Give the position of every malaria parasite and every leukocyte.
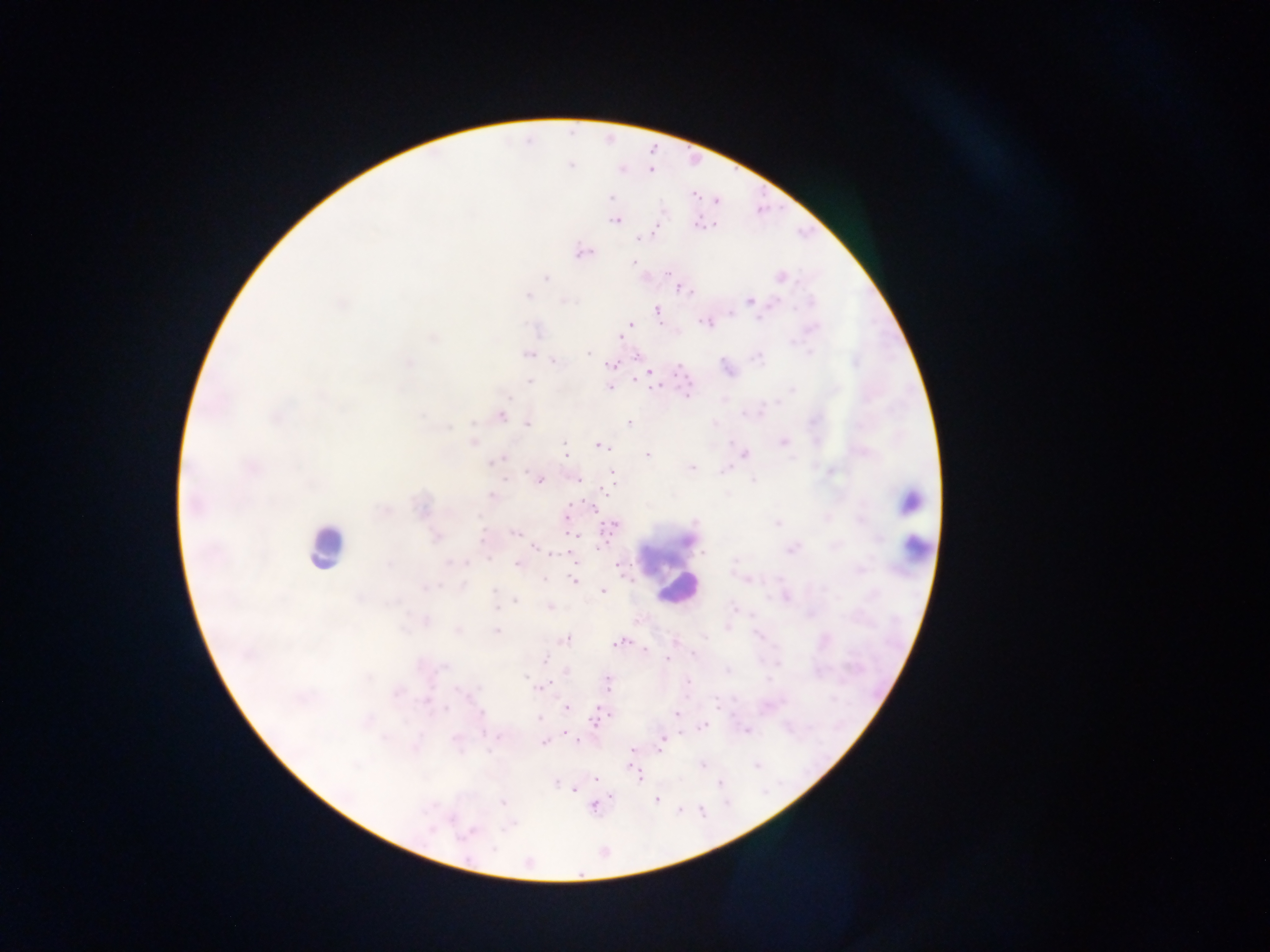
Approximate centers as (x, y) in pixels.
Malaria parasites: (571, 166), (650, 172), (611, 197), (694, 198), (616, 220), (698, 220), (653, 235), (637, 239), (583, 251), (633, 262), (680, 292), (750, 299), (657, 310), (732, 312), (760, 320), (630, 323), (622, 338), (590, 352), (534, 354), (757, 357), (554, 362), (610, 365), (650, 374), (528, 382), (654, 387), (609, 388), (687, 394), (502, 417), (528, 423), (629, 424), (564, 446), (601, 447), (566, 454), (746, 455), (647, 456), (693, 467), (613, 472), (505, 480), (542, 481), (578, 481), (607, 492), (908, 502), (592, 509), (567, 517), (860, 520), (611, 526), (514, 534), (570, 536), (877, 540), (482, 541), (602, 546), (534, 547), (701, 553), (489, 559), (572, 562), (516, 565), (618, 565), (545, 580), (573, 582), (496, 589), (426, 590), (603, 591), (514, 600), (550, 606), (496, 609), (496, 630), (627, 638), (566, 640), (614, 646), (645, 648), (544, 659), (668, 661), (566, 671), (606, 682), (689, 682), (416, 701), (566, 708), (597, 708), (446, 711), (676, 715), (609, 717), (539, 719), (594, 727), (699, 730), (567, 734), (543, 741), (579, 741), (633, 749), (660, 751), (632, 764), (594, 781), (640, 781), (555, 783), (720, 783), (574, 789), (609, 796), (655, 801), (503, 803), (682, 808).
Leukocytes: (319, 554), (913, 554), (672, 592).

Summary:
  - Field of view: single
  - Image size: 1270×952 pixels
  - Country: Ghana
  - Preparation: thick blood film
  - Capture: mobile-phone photograph through a microscope